Identify the parasite.
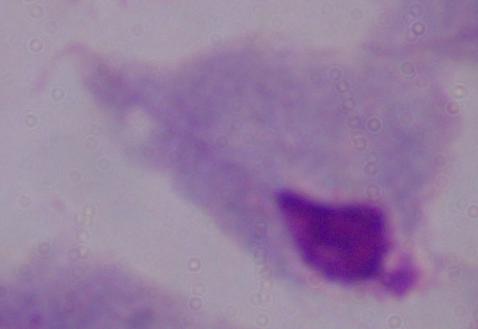

A trichomonad.

modality: photomicrograph
magnification: 1000x